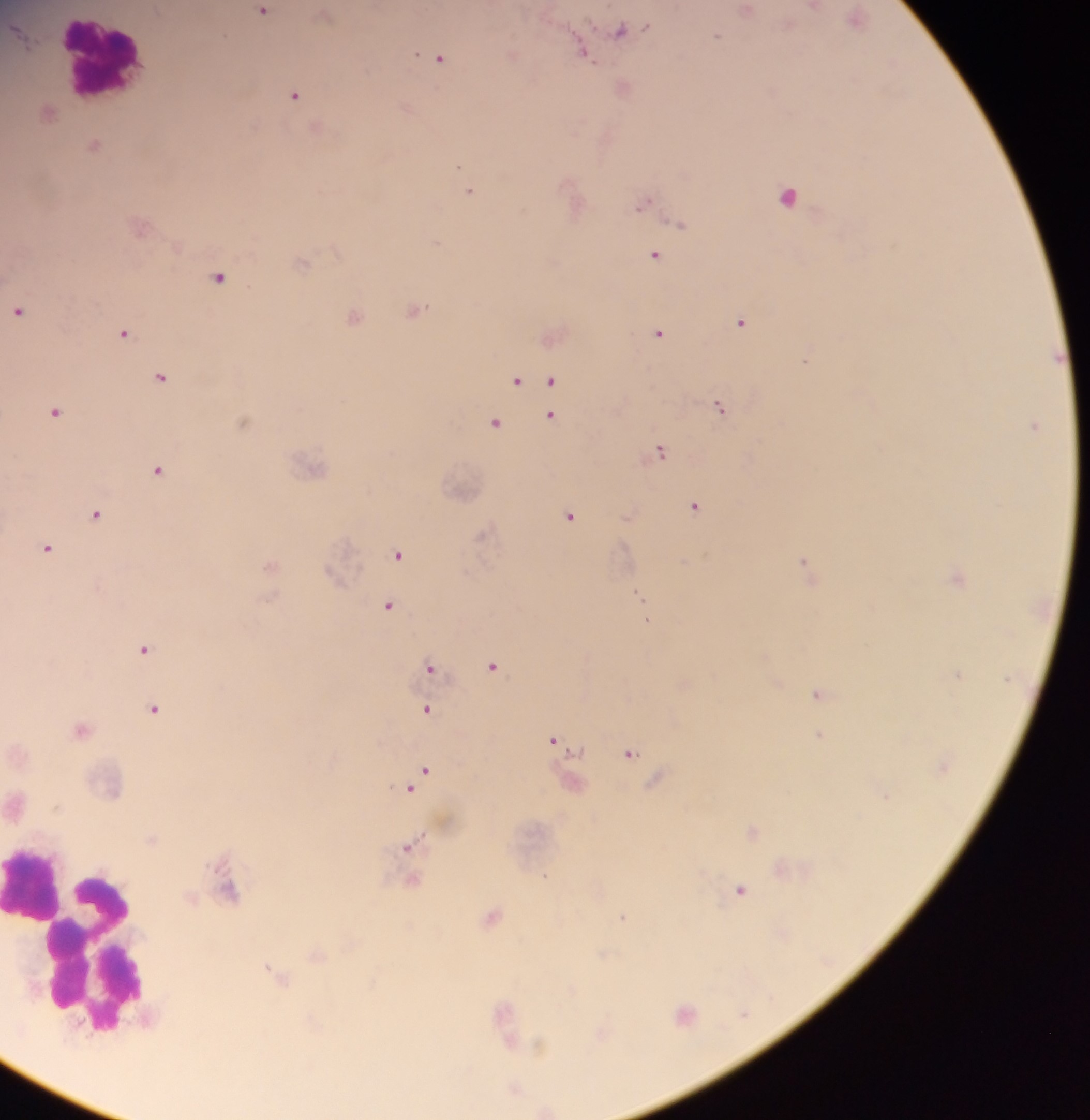
leukocyte_locations: 'approximate centers as [x, y] in pixels: [105, 59], [33, 887], [86, 963]'
image_size: 1090×1120 pixels
country: Ghana
field_of_view: single
capture: mobile-phone photograph through a microscope
preparation: thick blood smear
malaria_parasite_locations: 'approximate centers as [x, y] in pixels: [813, 6], [745, 10], [264, 11], [325, 14], [856, 17], [621, 29], [716, 36], [584, 53], [513, 54], [439, 57], [623, 86], [294, 94], [48, 111], [94, 144], [471, 192], [787, 196], [643, 202], [679, 223], [139, 225], [654, 255], [300, 264], [219, 276], [414, 309], [18, 310], [353, 316], [741, 322], [658, 332], [123, 333], [551, 334], [806, 359], [160, 375], [516, 380], [552, 380], [720, 406], [54, 411], [551, 416], [242, 421], [495, 421], [1034, 425], [660, 451], [311, 465], [156, 470], [694, 506], [96, 514], [570, 515], [628, 515], [485, 535], [48, 547], [399, 555], [804, 562], [270, 566], [808, 571], [958, 577], [639, 595], [389, 604], [647, 620], [144, 649], [492, 666], [430, 668], [958, 674], [429, 681], [818, 695], [153, 709], [428, 710], [81, 728], [820, 735], [554, 739], [629, 753], [421, 774], [657, 779], [571, 781], [414, 784], [17, 803], [752, 831], [409, 846], [411, 879], [740, 890], [228, 891], [492, 916], [622, 916], [317, 954], [277, 975], [685, 1014], [505, 1019], [540, 1045], [514, 1089], [546, 1110]'